Outline platelets.
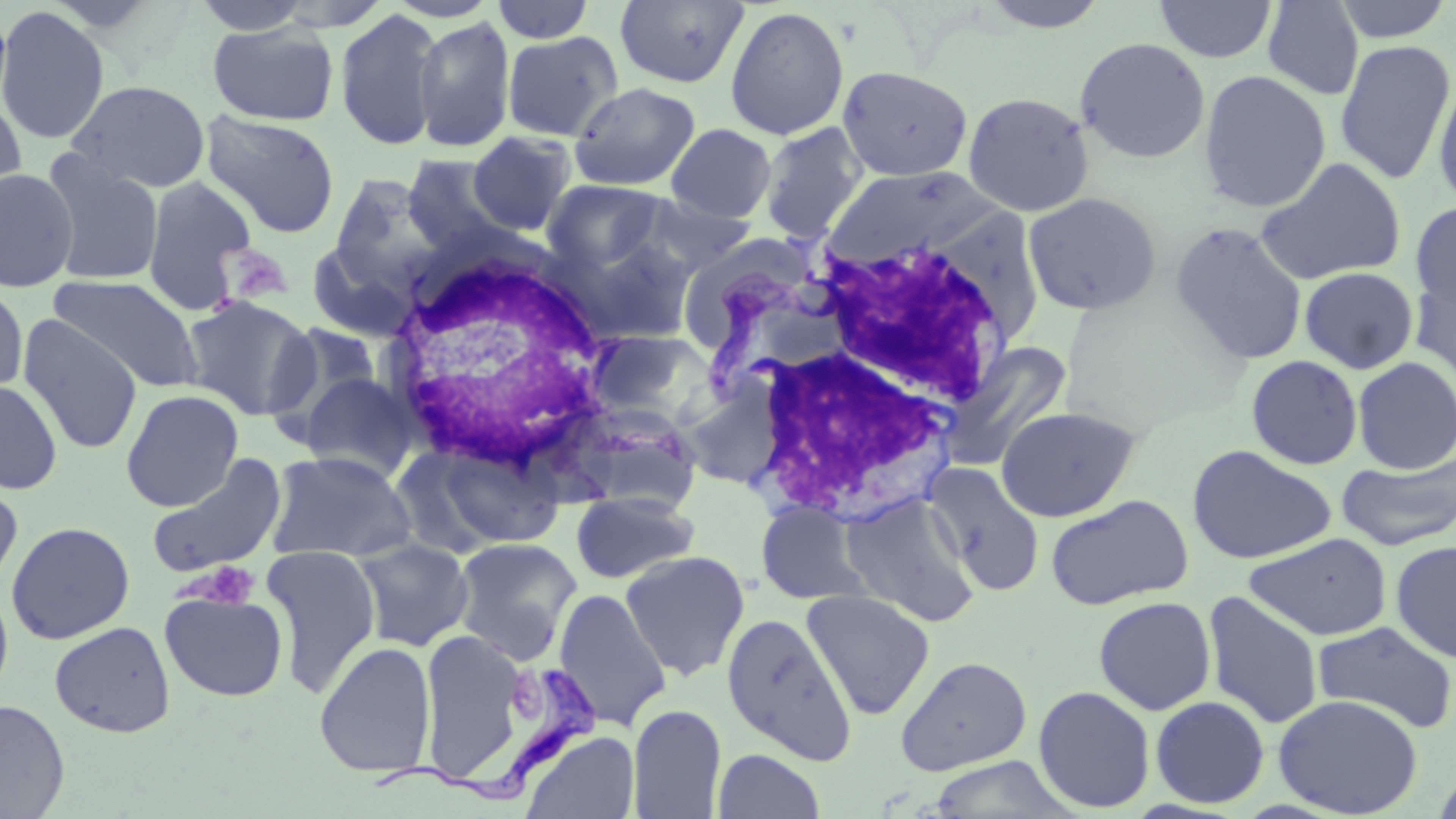

Approximate bounding boxes as named x1/y1/x2/y2 corners in pixels.
Platelets: (x1=189, y1=562, x2=259, y2=608).

White blood cell locations: (x1=812, y1=237, x2=1020, y2=411), (x1=382, y1=242, x2=621, y2=475), (x1=723, y1=324, x2=967, y2=527). Trypanosoma brucei locations: (x1=366, y1=664, x2=606, y2=804). Uninfected red blood cell locations: (x1=614, y1=0, x2=750, y2=88), (x1=978, y1=0, x2=1112, y2=33), (x1=1155, y1=0, x2=1277, y2=63), (x1=1330, y1=0, x2=1454, y2=43), (x1=187, y1=1, x2=317, y2=36), (x1=490, y1=1, x2=596, y2=44), (x1=1261, y1=1, x2=1365, y2=100), (x1=724, y1=5, x2=849, y2=141), (x1=0, y1=6, x2=110, y2=145), (x1=333, y1=8, x2=445, y2=151), (x1=413, y1=16, x2=515, y2=153), (x1=206, y1=22, x2=338, y2=126), (x1=502, y1=31, x2=624, y2=142), (x1=1074, y1=37, x2=1211, y2=164), (x1=1334, y1=38, x2=1455, y2=186), (x1=838, y1=65, x2=973, y2=181), (x1=1198, y1=69, x2=1332, y2=213), (x1=1433, y1=75, x2=1456, y2=209), (x1=67, y1=79, x2=211, y2=193), (x1=569, y1=82, x2=701, y2=191), (x1=0, y1=88, x2=28, y2=213), (x1=962, y1=91, x2=1095, y2=216), (x1=200, y1=110, x2=340, y2=238), (x1=759, y1=122, x2=868, y2=243), (x1=665, y1=123, x2=777, y2=223), (x1=466, y1=131, x2=578, y2=237), (x1=40, y1=150, x2=164, y2=287), (x1=403, y1=154, x2=515, y2=257), (x1=1256, y1=157, x2=1407, y2=286), (x1=823, y1=165, x2=994, y2=267), (x1=0, y1=168, x2=80, y2=292), (x1=329, y1=174, x2=448, y2=293), (x1=142, y1=175, x2=258, y2=314), (x1=542, y1=179, x2=669, y2=272), (x1=1023, y1=192, x2=1162, y2=315), (x1=641, y1=193, x2=759, y2=275), (x1=1410, y1=200, x2=1456, y2=316), (x1=1170, y1=221, x2=1308, y2=364), (x1=563, y1=233, x2=698, y2=345), (x1=307, y1=241, x2=418, y2=342), (x1=1300, y1=266, x2=1419, y2=374), (x1=1411, y1=269, x2=1456, y2=390), (x1=49, y1=274, x2=203, y2=393), (x1=0, y1=283, x2=29, y2=397), (x1=180, y1=294, x2=319, y2=420), (x1=17, y1=315, x2=143, y2=454), (x1=265, y1=321, x2=388, y2=438), (x1=585, y1=328, x2=719, y2=427), (x1=947, y1=342, x2=1073, y2=467), (x1=1246, y1=355, x2=1363, y2=469), (x1=1352, y1=356, x2=1456, y2=474), (x1=297, y1=371, x2=420, y2=482), (x1=0, y1=379, x2=63, y2=495), (x1=121, y1=389, x2=244, y2=511), (x1=559, y1=403, x2=703, y2=516), (x1=996, y1=405, x2=1142, y2=522), (x1=413, y1=439, x2=566, y2=552), (x1=1186, y1=444, x2=1337, y2=564), (x1=265, y1=449, x2=417, y2=563), (x1=146, y1=453, x2=288, y2=576), (x1=1337, y1=455, x2=1456, y2=550), (x1=925, y1=462, x2=1045, y2=597), (x1=0, y1=479, x2=23, y2=594), (x1=840, y1=491, x2=979, y2=625), (x1=571, y1=492, x2=699, y2=584), (x1=1045, y1=493, x2=1194, y2=610), (x1=756, y1=499, x2=872, y2=605), (x1=6, y1=521, x2=135, y2=644), (x1=1244, y1=532, x2=1393, y2=641), (x1=352, y1=537, x2=474, y2=652), (x1=452, y1=537, x2=582, y2=663), (x1=1391, y1=539, x2=1456, y2=664), (x1=261, y1=545, x2=382, y2=695), (x1=619, y1=550, x2=750, y2=680), (x1=0, y1=582, x2=14, y2=703), (x1=553, y1=587, x2=671, y2=731), (x1=801, y1=588, x2=935, y2=720), (x1=159, y1=589, x2=288, y2=702), (x1=1202, y1=591, x2=1324, y2=729), (x1=1093, y1=596, x2=1216, y2=715), (x1=721, y1=612, x2=857, y2=764), (x1=1312, y1=620, x2=1456, y2=733), (x1=49, y1=621, x2=175, y2=737), (x1=419, y1=629, x2=526, y2=779), (x1=314, y1=641, x2=437, y2=777), (x1=895, y1=656, x2=1033, y2=776), (x1=1033, y1=685, x2=1156, y2=813), (x1=1273, y1=694, x2=1423, y2=817), (x1=1150, y1=695, x2=1270, y2=808), (x1=0, y1=698, x2=70, y2=818), (x1=628, y1=704, x2=726, y2=818), (x1=521, y1=729, x2=639, y2=819), (x1=713, y1=748, x2=825, y2=819), (x1=925, y1=755, x2=1082, y2=818), (x1=1433, y1=765, x2=1456, y2=819). Slide-level diagnosis: Trypanosoma brucei. Single field of view. 1000x magnification. Optical microscopy. Thin blood film. Image is 1456×819 pixels. May-Grünwald-Giemsa-stained preparation.